Assess for parasitized red blood cells.
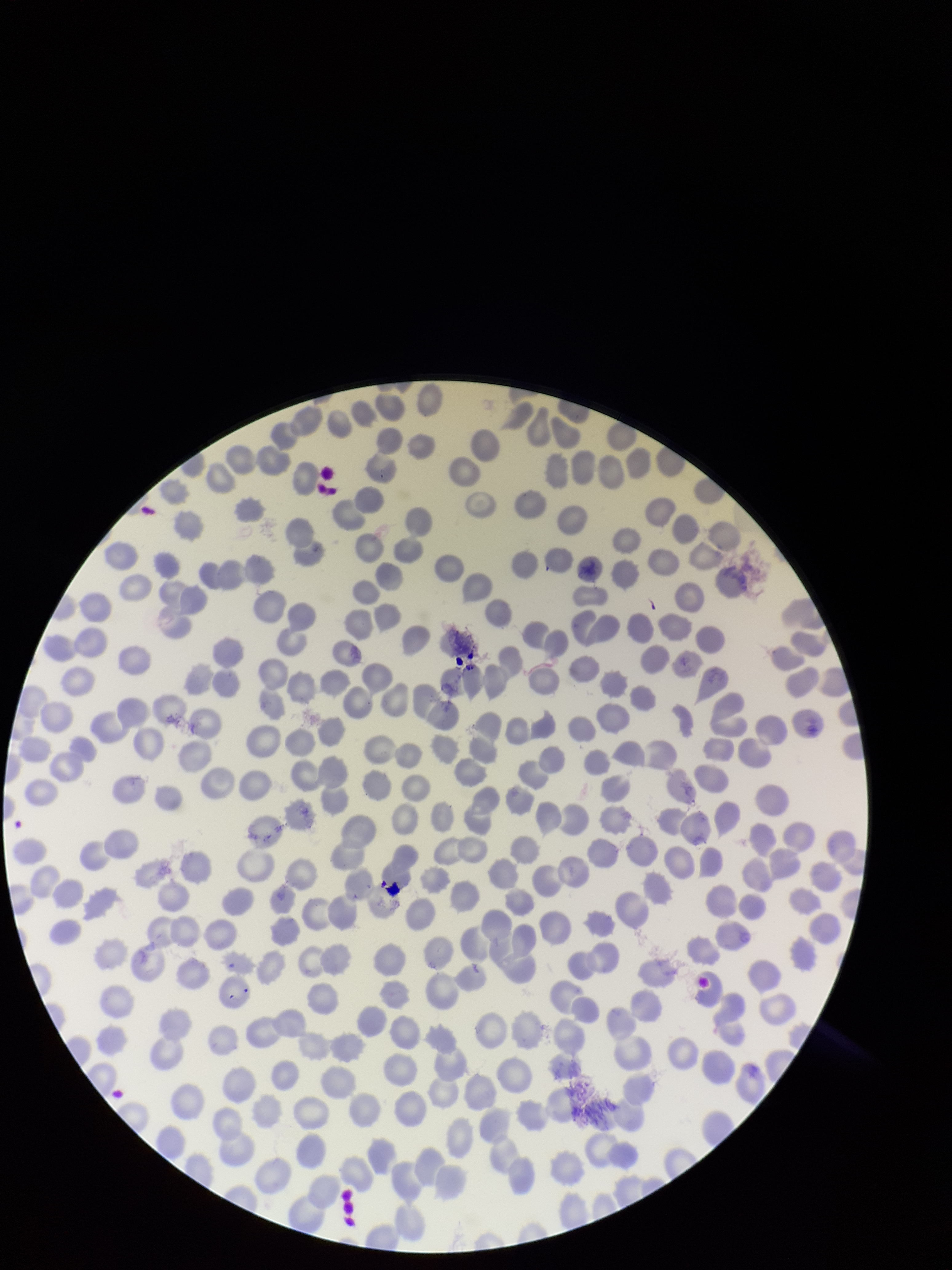

None identified.

Patient malaria status: infected. Parasitized red blood cell count: 0. Red blood cell count: 286. Species reported for this patient: Plasmodium falciparum. Image is 952×1270 pixels. Single field of view. Preparation: thin. Stained with Giemsa. Smartphone photograph taken through the eyepiece of a microscope.